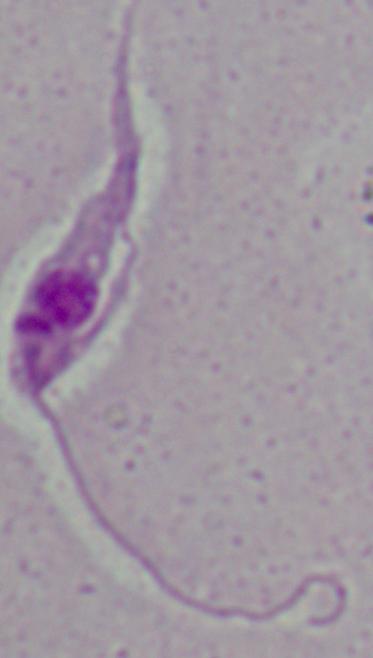

modality: photomicrograph
magnification: 1000x
identification: Leishmania